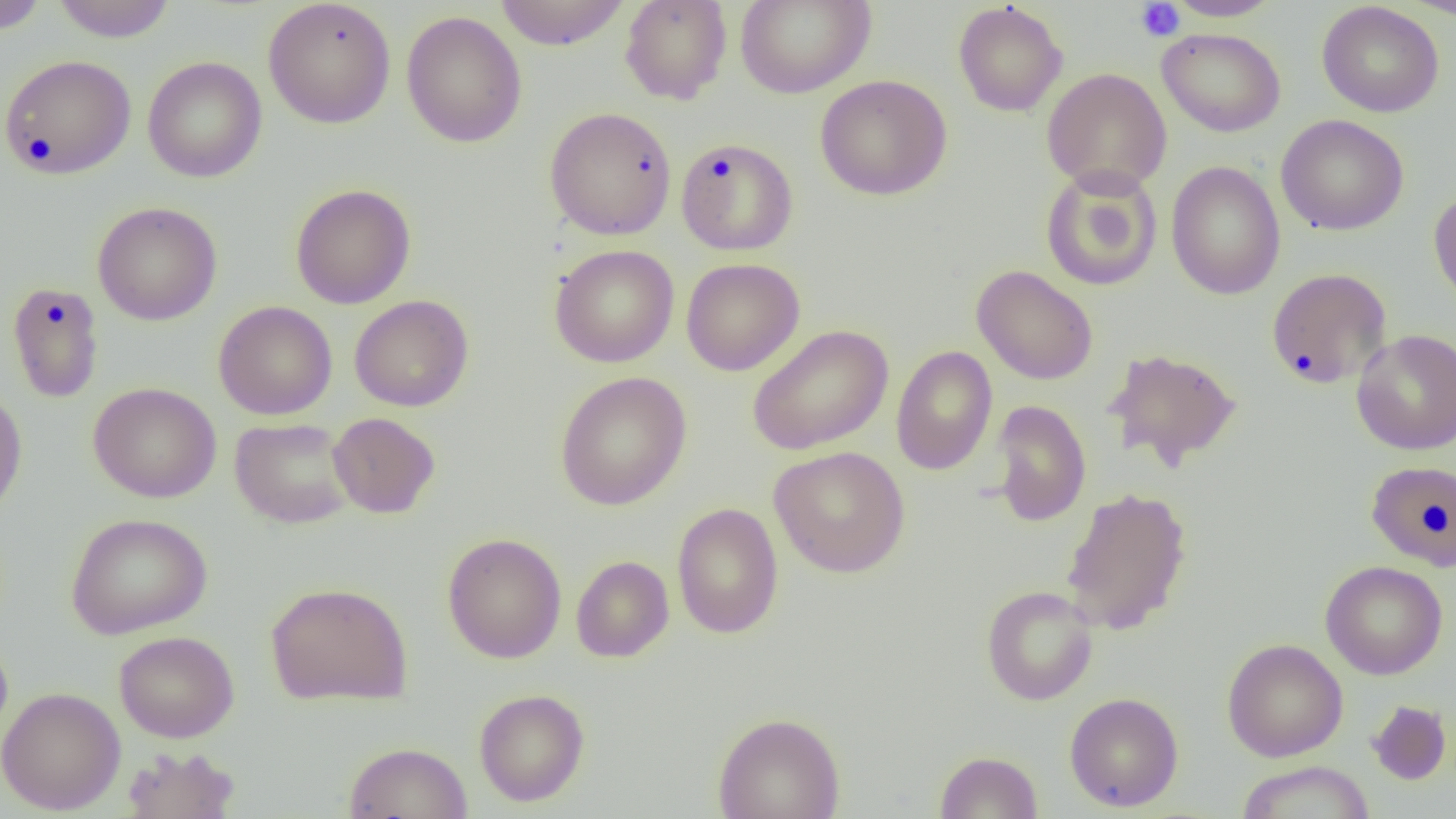
slide_level_diagnosis: negative for blood parasites
modality: light microscopy
field_of_view: one of a larger specimen
uninfected_red_blood_cell_locations: 'approximate bounding boxes as (x1, y1, x2, y2) in pixels: (0, 0, 48, 34), (51, 0, 177, 42), (263, 0, 396, 128), (494, 0, 631, 50), (619, 0, 732, 105), (735, 0, 874, 99), (1164, 0, 1284, 22), (1400, 0, 1456, 19), (952, 2, 1068, 117), (1316, 2, 1445, 117), (401, 11, 527, 148), (1157, 27, 1285, 137), (0, 54, 136, 179), (142, 56, 267, 183), (1041, 68, 1172, 196), (814, 74, 952, 201), (544, 106, 677, 240), (1276, 114, 1409, 236), (676, 137, 799, 256), (1166, 161, 1285, 301), (1041, 166, 1162, 291), (290, 184, 416, 309), (1428, 187, 1456, 310), (93, 201, 222, 326), (550, 244, 679, 368), (681, 258, 805, 376), (971, 265, 1098, 385), (1266, 267, 1393, 389), (6, 280, 105, 404), (350, 295, 474, 412), (213, 301, 337, 420), (747, 324, 893, 456), (1351, 328, 1456, 454), (891, 345, 998, 475), (1103, 348, 1243, 470), (554, 371, 692, 511), (88, 382, 221, 503), (0, 387, 27, 517), (989, 399, 1091, 527), (328, 412, 440, 519), (230, 417, 358, 529), (769, 446, 910, 578), (1366, 462, 1455, 570), (1060, 486, 1193, 636), (671, 503, 784, 639), (65, 513, 212, 639), (442, 532, 567, 663), (571, 555, 674, 662), (1321, 560, 1448, 680), (265, 581, 413, 706), (981, 585, 1098, 705), (114, 631, 239, 743), (0, 636, 13, 748), (1222, 638, 1348, 762), (0, 686, 125, 814), (474, 689, 590, 806), (1065, 692, 1184, 811), (1366, 699, 1453, 785), (712, 711, 846, 819), (343, 741, 472, 819), (122, 746, 241, 819), (934, 751, 1043, 818), (1235, 760, 1375, 819)'
preparation: thin blood smear
platelet_locations: 'approximate bounding boxes as (x1, y1, x2, y2) in pixels: (1135, 1, 1185, 41)'
image_size: 1456×819 pixels
magnification: 1000x